Classify this cell by malaria status.
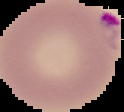

Parasitized.

image size = 124×112 pixels
preparation = thin blood film
image type = cell region segmented out of the field of view; surrounding area masked to black